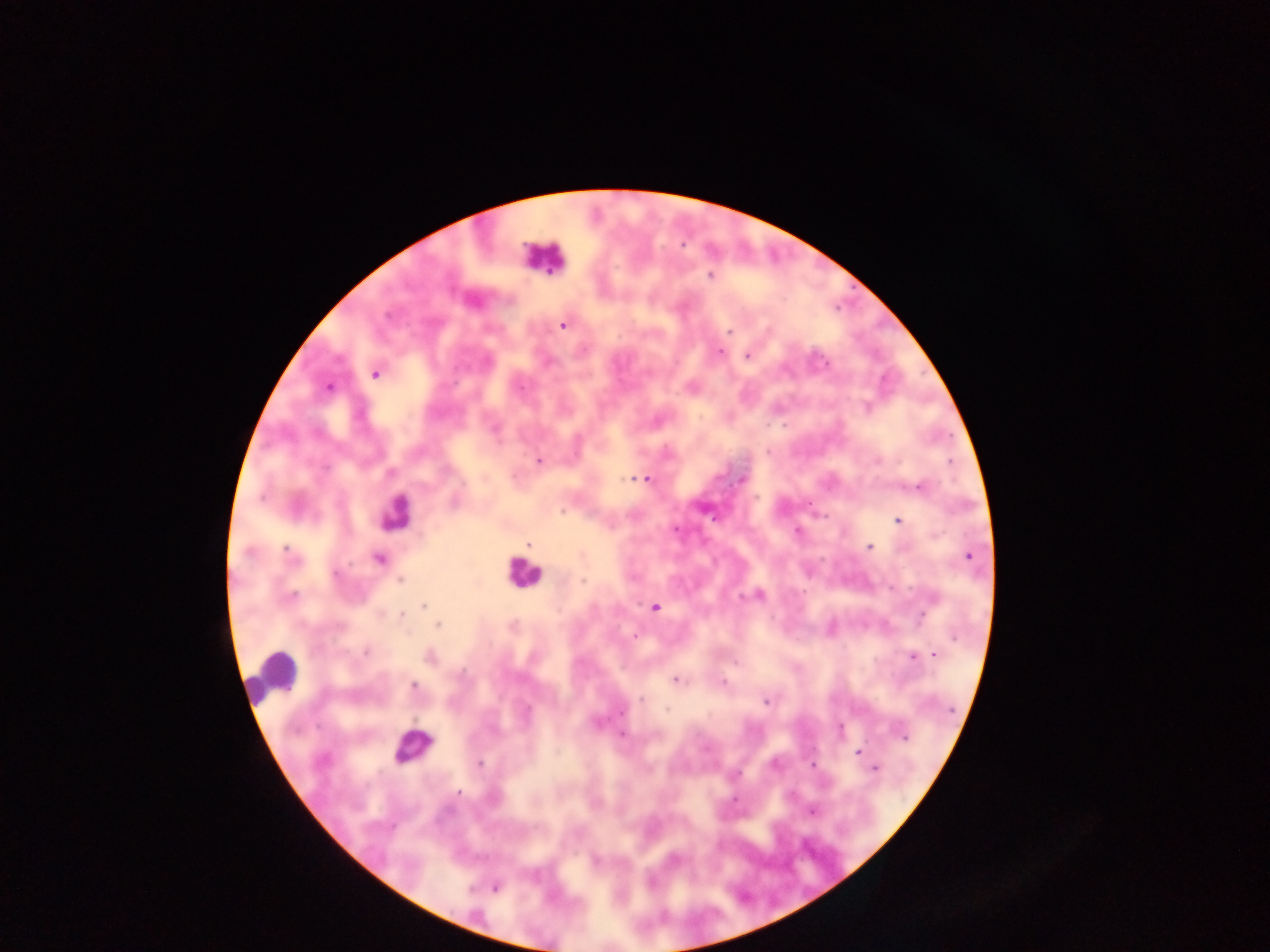

Approximate centers as {x, y} in pixels. Plasmodium parasite locations: {710, 275}, {563, 325}, {729, 332}, {719, 351}, {747, 356}, {375, 374}, {328, 387}, {521, 387}, {867, 408}, {495, 429}, {768, 452}, {876, 460}, {539, 461}, {631, 478}, {743, 478}, {645, 479}, {919, 486}, {563, 512}, {712, 518}, {898, 521}, {797, 531}, {527, 545}, {869, 546}, {287, 551}, {249, 554}, {970, 557}, {379, 558}, {335, 573}, {400, 580}, {583, 580}, {759, 595}, {292, 597}, {741, 597}, {423, 606}, {655, 607}, {402, 615}, {922, 617}, {438, 625}, {635, 636}, {366, 652}, {935, 655}, {430, 657}, {912, 657}, {675, 681}, {724, 682}, {414, 686}, {643, 699}, {765, 702}, {667, 710}, {621, 712}, {840, 729}, {622, 735}, {904, 736}, {859, 753}, {479, 763}, {875, 769}, {458, 793}, {812, 812}, {675, 858}, {596, 860}, {496, 887}. Leukocyte locations: {542, 256}, {395, 512}, {522, 573}, {273, 676}, {407, 746}. Image is 1270×952 pixels. Sample from Ghana. Mobile-phone photograph taken through the microscope. One field of view. Thick blood film.